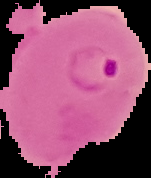

malaria status = parasitized
preparation = thin blood film
image type = segmented cell region on a black background
image size = 151×178 pixels